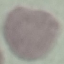

Summary:
  - Result: no malaria parasites seen
  - Preparation: thin smear
  - Capture: smartphone camera at the microscope eyepiece
  - Stain: Giemsa
  - Image type: cell patch, automatically extracted from a larger field of view and resized to 64 × 64 pixels